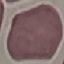

result = no malaria parasites seen
preparation = thin smear
capture = smartphone camera at the microscope eyepiece
stain = Giemsa
image type = automatically extracted cell patch, resized to 64 × 64 pixels